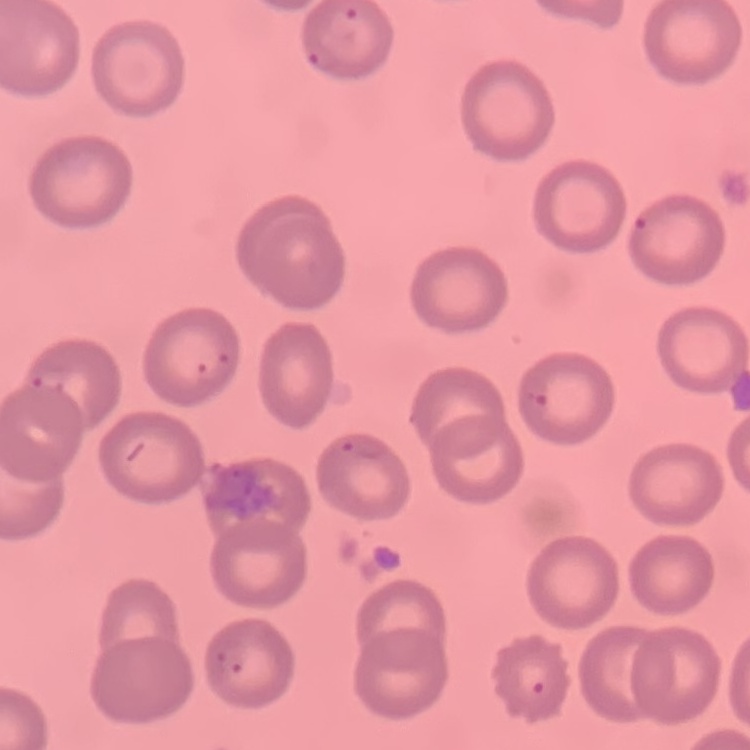

The red blood cells exhibit no rouleaux formation. Stained with either Field's or Giemsa. Square crop of a larger photomicrograph. Thin blood smear.